Assess this cell for malaria.
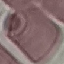

It is uninfected.

capture = smartphone through the microscope eyepiece
stain = Giemsa
image type = automatically extracted cell patch, resized to 64 × 64 pixels
preparation = thin blood film